Evaluate for malaria.
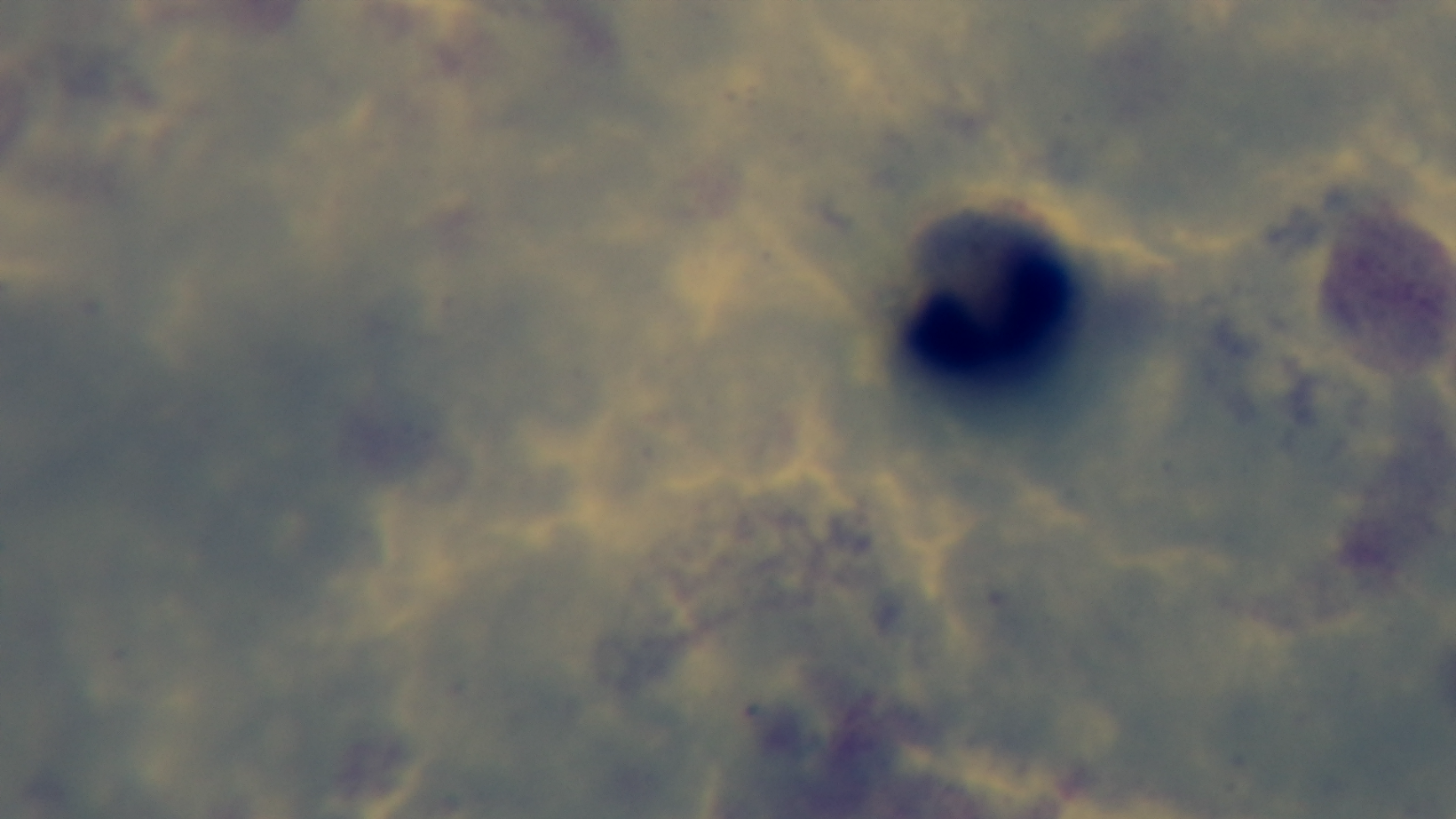

Uninfected.

field_of_view: one from the slide
capture: mounted 4K digital camera
modality: light microscopy
stain: Giemsa
preparation: thick blood film
objective: 100x oil immersion